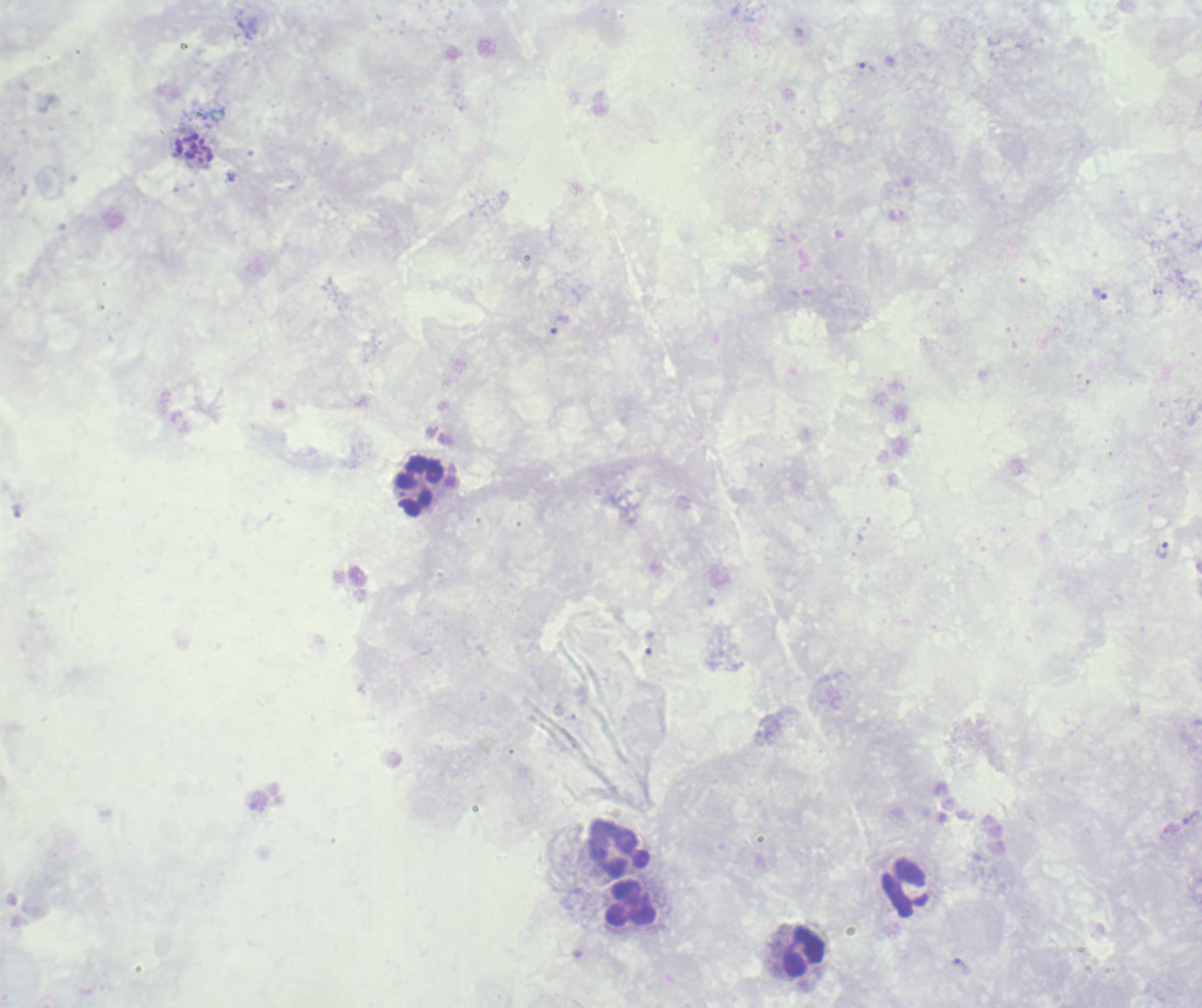

Approximate centers as [x, y] in pixels.
Summary:
  - Trophozoite locations: [1099, 294], [561, 325], [1162, 551], [649, 643], [961, 966]
  - Schizont locations: [194, 149]
  - Leukocyte locations: [419, 487], [619, 849], [632, 905], [804, 952]
  - Life-cycle stages observed: trophozoite, schizont
  - Context: previously used in an actual diagnosis
  - Image size: 1202×1008 pixels
  - Background quality: poor
  - Magnification: 100x
  - Field of view: one from this slide
  - Stain: Romanowsky
  - Preparation: thick blood film
  - Result: positive for Plasmodium parasites